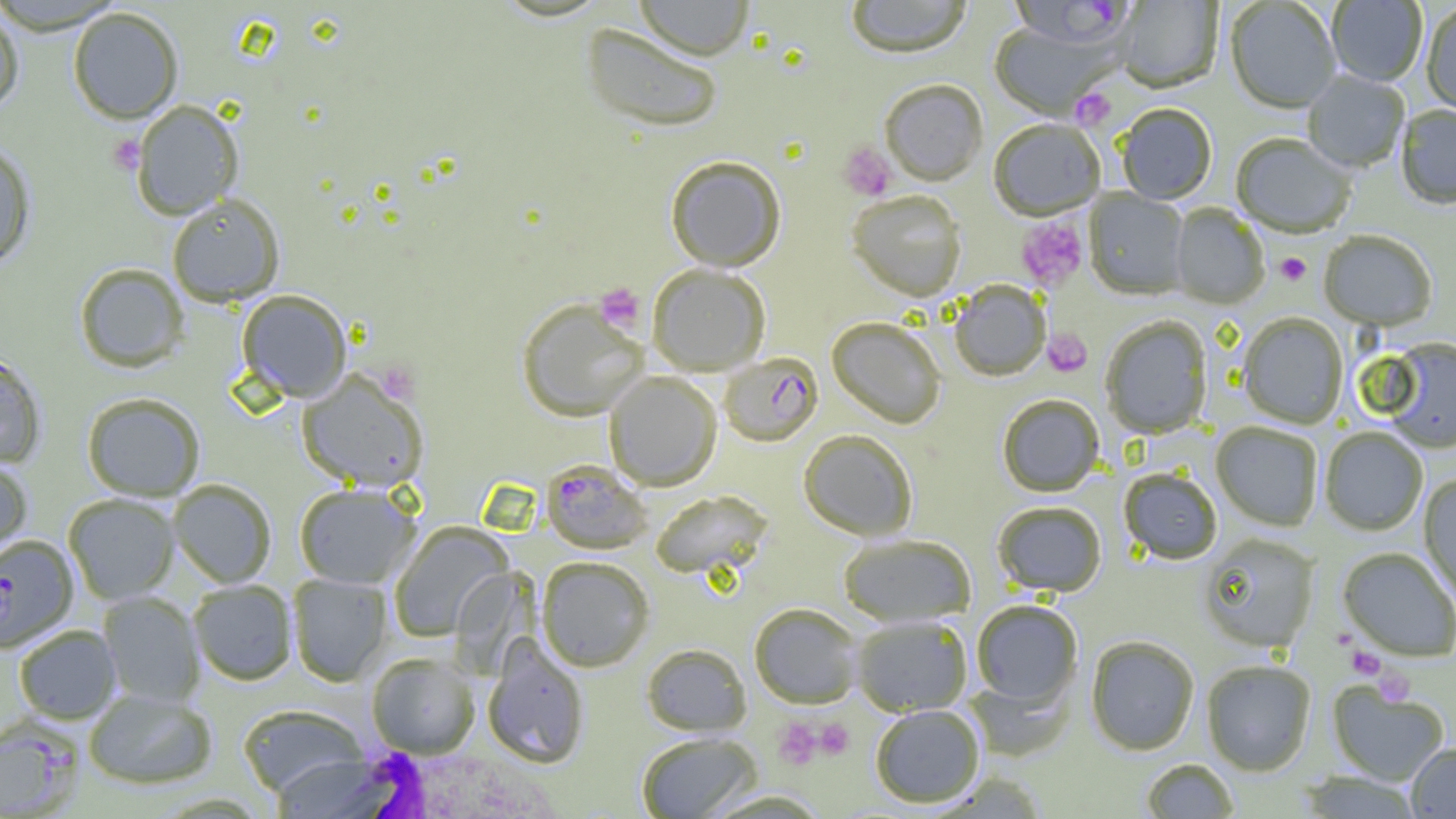
{
  "plasmodium_falciparum_infected_red_blood_cell_locations": "approximate bounding boxes as named x1/y1/x2/y2 corners in pixels: (x1=1008, y1=0, x2=1133, y2=51), (x1=719, y1=353, x2=823, y2=447), (x1=541, y1=459, x2=653, y2=554), (x1=0, y1=533, x2=77, y2=651), (x1=0, y1=719, x2=81, y2=819)",
  "slide_level_diagnosis": "Plasmodium falciparum",
  "white_blood_cell_locations": "approximate bounding boxes as named x1/y1/x2/y2 corners in pixels: (x1=328, y1=744, x2=565, y2=819)",
  "image_size": "1456×819 pixels",
  "modality": "light microscopy",
  "magnification": "1000x",
  "field_of_view": "single",
  "uninfected_red_blood_cell_locations": "approximate bounding boxes as named x1/y1/x2/y2 corners in pixels: (x1=635, y1=0, x2=754, y2=61), (x1=845, y1=0, x2=972, y2=59), (x1=1114, y1=0, x2=1223, y2=94), (x1=1225, y1=1, x2=1341, y2=114), (x1=1327, y1=1, x2=1427, y2=87), (x1=1422, y1=4, x2=1456, y2=117), (x1=0, y1=6, x2=25, y2=114), (x1=68, y1=6, x2=183, y2=124), (x1=581, y1=22, x2=724, y2=133), (x1=988, y1=24, x2=1119, y2=120), (x1=1303, y1=72, x2=1409, y2=174), (x1=879, y1=80, x2=987, y2=187), (x1=131, y1=100, x2=244, y2=219), (x1=1116, y1=105, x2=1217, y2=205), (x1=1396, y1=106, x2=1455, y2=210), (x1=989, y1=120, x2=1105, y2=222), (x1=1231, y1=135, x2=1354, y2=239), (x1=0, y1=141, x2=36, y2=269), (x1=665, y1=155, x2=786, y2=272), (x1=1084, y1=189, x2=1189, y2=301), (x1=846, y1=191, x2=966, y2=302), (x1=167, y1=193, x2=285, y2=307), (x1=1171, y1=204, x2=1268, y2=309), (x1=1319, y1=231, x2=1437, y2=332), (x1=74, y1=263, x2=189, y2=373), (x1=648, y1=264, x2=770, y2=376), (x1=949, y1=281, x2=1050, y2=382), (x1=237, y1=289, x2=352, y2=402), (x1=517, y1=298, x2=649, y2=421), (x1=1238, y1=313, x2=1348, y2=429), (x1=1100, y1=316, x2=1212, y2=439), (x1=827, y1=318, x2=946, y2=429), (x1=1382, y1=339, x2=1456, y2=454), (x1=0, y1=352, x2=46, y2=468), (x1=296, y1=370, x2=429, y2=492), (x1=604, y1=371, x2=721, y2=490), (x1=82, y1=392, x2=205, y2=501), (x1=997, y1=394, x2=1104, y2=497), (x1=1211, y1=422, x2=1322, y2=531), (x1=1320, y1=428, x2=1428, y2=536), (x1=798, y1=429, x2=917, y2=541), (x1=0, y1=457, x2=33, y2=567), (x1=1119, y1=468, x2=1222, y2=564), (x1=1418, y1=474, x2=1456, y2=606), (x1=168, y1=479, x2=277, y2=588), (x1=294, y1=483, x2=420, y2=588), (x1=651, y1=490, x2=774, y2=581), (x1=63, y1=493, x2=179, y2=604), (x1=992, y1=501, x2=1106, y2=598), (x1=388, y1=522, x2=514, y2=642), (x1=838, y1=534, x2=977, y2=627), (x1=1198, y1=535, x2=1319, y2=653), (x1=1338, y1=548, x2=1456, y2=662), (x1=536, y1=556, x2=654, y2=671), (x1=287, y1=573, x2=392, y2=686), (x1=188, y1=579, x2=297, y2=685), (x1=98, y1=591, x2=204, y2=707), (x1=971, y1=600, x2=1083, y2=709), (x1=750, y1=603, x2=863, y2=709), (x1=851, y1=616, x2=972, y2=716), (x1=13, y1=624, x2=122, y2=725), (x1=1086, y1=636, x2=1199, y2=755), (x1=482, y1=637, x2=589, y2=768), (x1=641, y1=643, x2=752, y2=737), (x1=367, y1=652, x2=480, y2=759), (x1=1202, y1=660, x2=1316, y2=776), (x1=1327, y1=683, x2=1449, y2=786), (x1=84, y1=688, x2=218, y2=791), (x1=238, y1=703, x2=368, y2=797), (x1=870, y1=705, x2=985, y2=808), (x1=635, y1=732, x2=762, y2=818), (x1=1406, y1=743, x2=1456, y2=818), (x1=267, y1=754, x2=388, y2=816), (x1=1141, y1=759, x2=1239, y2=818), (x1=1298, y1=772, x2=1423, y2=818), (x1=702, y1=789, x2=832, y2=818)",
  "preparation": "thin blood smear",
  "platelet_locations": "approximate bounding boxes as named x1/y1/x2/y2 corners in pixels: (x1=1071, y1=88, x2=1116, y2=130), (x1=108, y1=134, x2=144, y2=175), (x1=838, y1=142, x2=897, y2=202), (x1=1017, y1=217, x2=1088, y2=291), (x1=1275, y1=253, x2=1311, y2=286), (x1=594, y1=283, x2=646, y2=333), (x1=1043, y1=328, x2=1091, y2=377), (x1=375, y1=362, x2=420, y2=403), (x1=1333, y1=629, x2=1358, y2=652), (x1=1348, y1=647, x2=1384, y2=679), (x1=1373, y1=668, x2=1415, y2=706), (x1=814, y1=718, x2=854, y2=759), (x1=773, y1=719, x2=824, y2=769)"
}